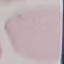
{
  "result": "no malaria parasites seen",
  "preparation": "thin blood smear",
  "capture": "smartphone through the microscope eyepiece",
  "image_type": "automatically extracted cell patch, resized to 64 × 64 pixels",
  "stain": "Giemsa"
}